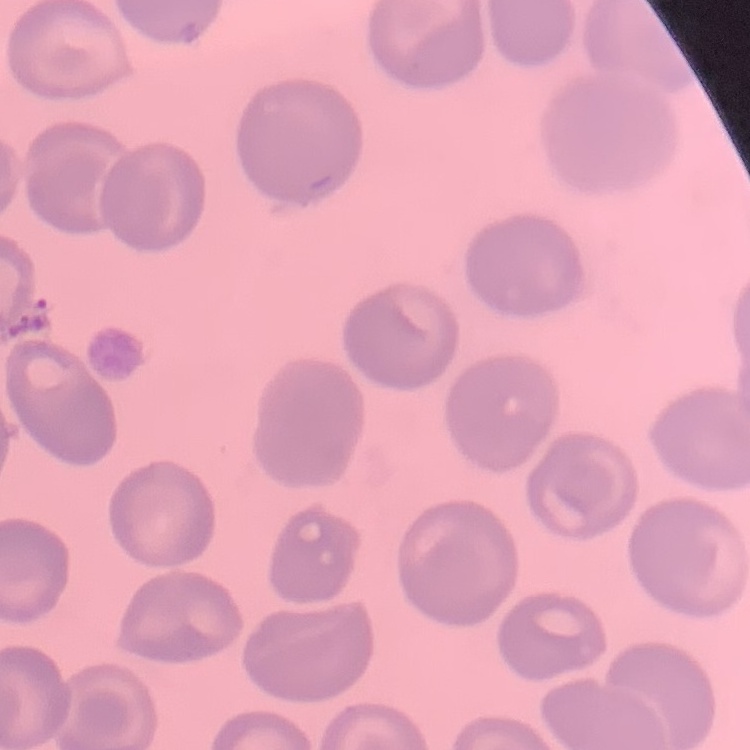

red blood cell morphology = no rouleaux formation
preparation = thin peripheral smear
stain = Field's or Giemsa
image type = one tile cut from a larger photomicrograph